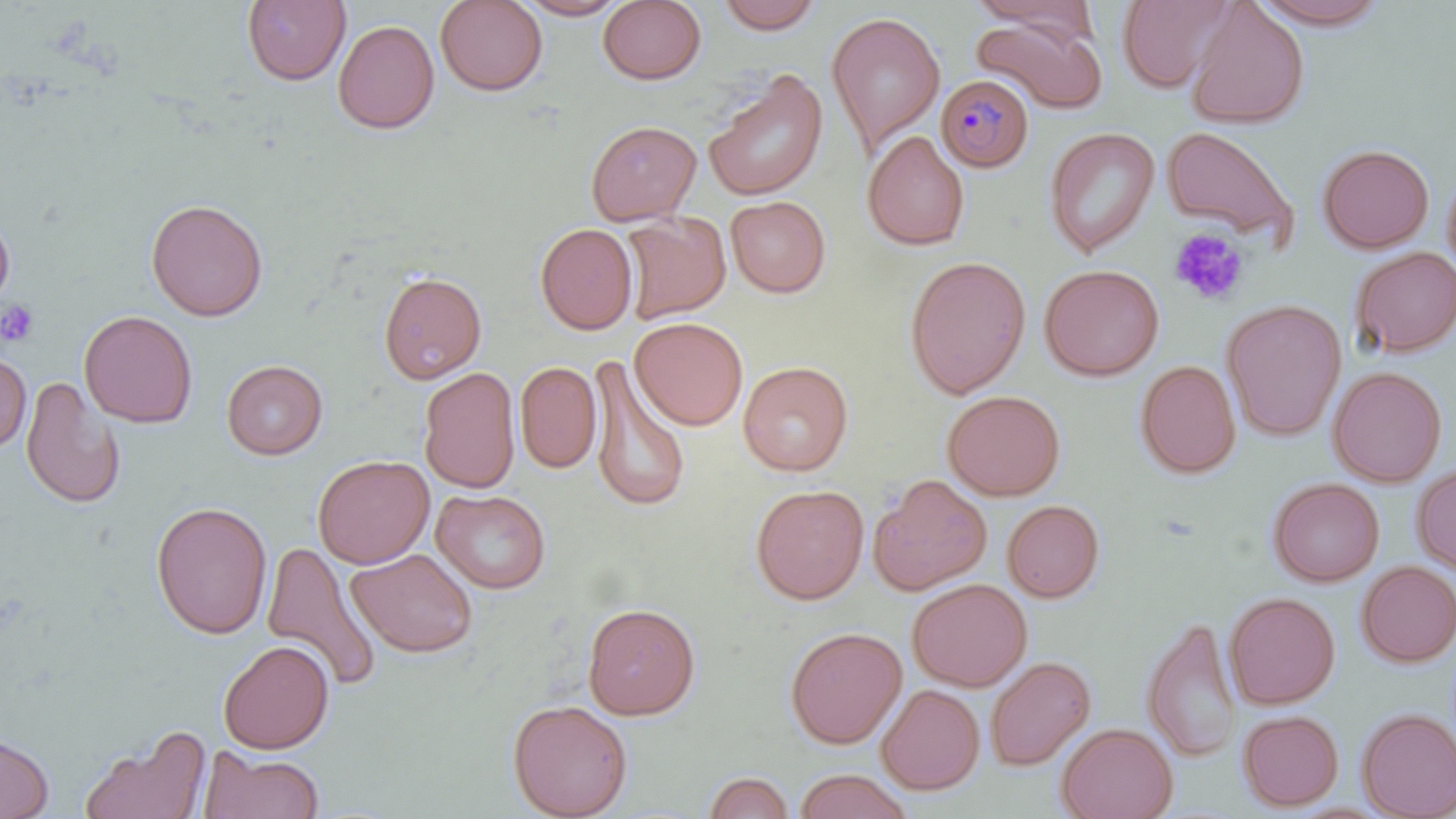
slide_level_diagnosis: Plasmodium malariae
image_size: 1456×819 pixels
stain: May-Grünwald-Giemsa
uninfected_red_blood_cell_locations: 'approximate bounding boxes as named x1/y1/x2/y2 corners in pixels: (x1=241, y1=0, x2=350, y2=86), (x1=434, y1=0, x2=548, y2=96), (x1=512, y1=0, x2=630, y2=20), (x1=598, y1=0, x2=707, y2=85), (x1=713, y1=0, x2=826, y2=34), (x1=1116, y1=0, x2=1238, y2=93), (x1=1252, y1=0, x2=1392, y2=29), (x1=967, y1=1, x2=1094, y2=33), (x1=1185, y1=1, x2=1310, y2=129), (x1=826, y1=11, x2=945, y2=155), (x1=971, y1=14, x2=1106, y2=114), (x1=333, y1=20, x2=440, y2=134), (x1=704, y1=69, x2=828, y2=202), (x1=586, y1=119, x2=702, y2=225), (x1=1161, y1=125, x2=1299, y2=244), (x1=1043, y1=127, x2=1160, y2=257), (x1=862, y1=130, x2=970, y2=251), (x1=1317, y1=143, x2=1434, y2=253), (x1=1442, y1=168, x2=1456, y2=283), (x1=725, y1=195, x2=831, y2=298), (x1=145, y1=198, x2=268, y2=321), (x1=0, y1=210, x2=16, y2=314), (x1=619, y1=211, x2=731, y2=325), (x1=535, y1=223, x2=637, y2=335), (x1=1350, y1=246, x2=1456, y2=357), (x1=904, y1=254, x2=1032, y2=398), (x1=1039, y1=263, x2=1165, y2=381), (x1=378, y1=271, x2=487, y2=384), (x1=1221, y1=298, x2=1346, y2=441), (x1=79, y1=310, x2=198, y2=427), (x1=630, y1=317, x2=748, y2=430), (x1=0, y1=352, x2=31, y2=452), (x1=586, y1=357, x2=692, y2=514), (x1=221, y1=359, x2=328, y2=459), (x1=1134, y1=359, x2=1241, y2=479), (x1=515, y1=360, x2=601, y2=474), (x1=737, y1=360, x2=854, y2=476), (x1=1328, y1=366, x2=1447, y2=486), (x1=418, y1=367, x2=521, y2=493), (x1=20, y1=376, x2=126, y2=510), (x1=942, y1=389, x2=1066, y2=500), (x1=312, y1=454, x2=435, y2=569), (x1=1411, y1=463, x2=1456, y2=575), (x1=868, y1=474, x2=992, y2=595), (x1=1267, y1=477, x2=1384, y2=587), (x1=750, y1=484, x2=869, y2=604), (x1=431, y1=488, x2=551, y2=594), (x1=1002, y1=499, x2=1105, y2=602), (x1=151, y1=500, x2=272, y2=639), (x1=260, y1=539, x2=384, y2=693), (x1=347, y1=548, x2=478, y2=658), (x1=1356, y1=560, x2=1456, y2=667), (x1=907, y1=578, x2=1032, y2=691), (x1=1224, y1=591, x2=1340, y2=709), (x1=582, y1=602, x2=701, y2=720), (x1=1141, y1=615, x2=1241, y2=763), (x1=784, y1=626, x2=907, y2=749), (x1=217, y1=640, x2=335, y2=754), (x1=985, y1=655, x2=1096, y2=771), (x1=876, y1=683, x2=985, y2=795), (x1=507, y1=699, x2=633, y2=819), (x1=1356, y1=707, x2=1456, y2=818), (x1=1237, y1=709, x2=1344, y2=811), (x1=1056, y1=722, x2=1178, y2=819), (x1=79, y1=724, x2=212, y2=819), (x1=0, y1=732, x2=54, y2=818), (x1=199, y1=747, x2=325, y2=819), (x1=793, y1=770, x2=913, y2=819), (x1=704, y1=771, x2=795, y2=818)'
platelet_locations: 'approximate bounding boxes as named x1/y1/x2/y2 corners in pixels: (x1=1169, y1=227, x2=1249, y2=306), (x1=0, y1=299, x2=39, y2=346)'
magnification: 1000x
field_of_view: one of a larger specimen
plasmodium_malariae_infected_red_blood_cell_locations: 'approximate bounding boxes as named x1/y1/x2/y2 corners in pixels: (x1=936, y1=74, x2=1034, y2=173)'
modality: optical microscopy
preparation: thin blood smear